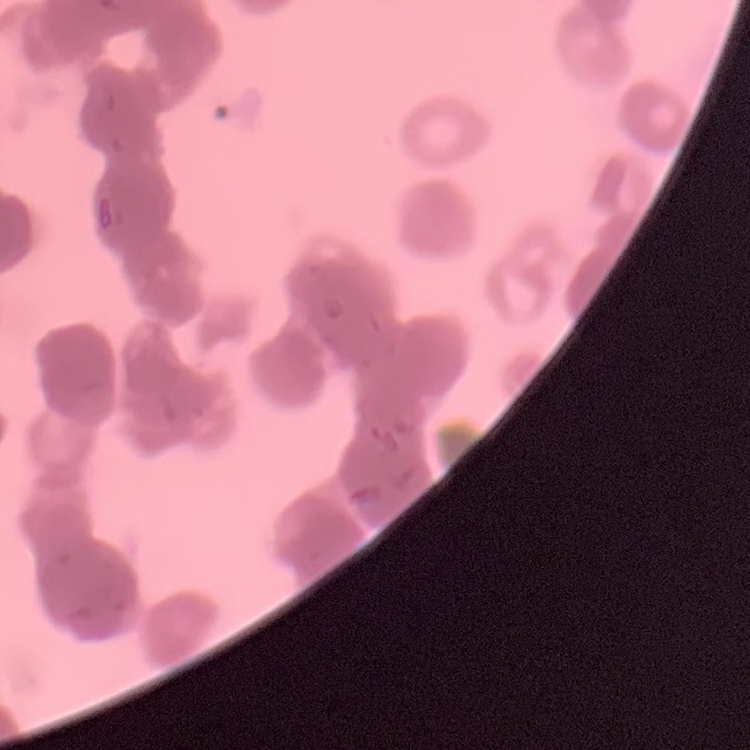

The erythrocytes show rouleaux formation. One tile cut from a larger photomicrograph. Thin blood film. Field's or Giemsa stain.